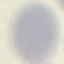 Malaria status: uninfected. Photographed with a smartphone camera at the microscope eyepiece. Thin blood smear. Cell patch, automatically extracted from a larger field of view and resized to 64 × 64 pixels. Giemsa stain.